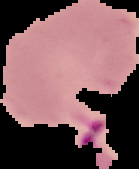

image size = 139×169 pixels
malaria status = parasitized
preparation = thin blood smear
image type = segmented cell region on a black background